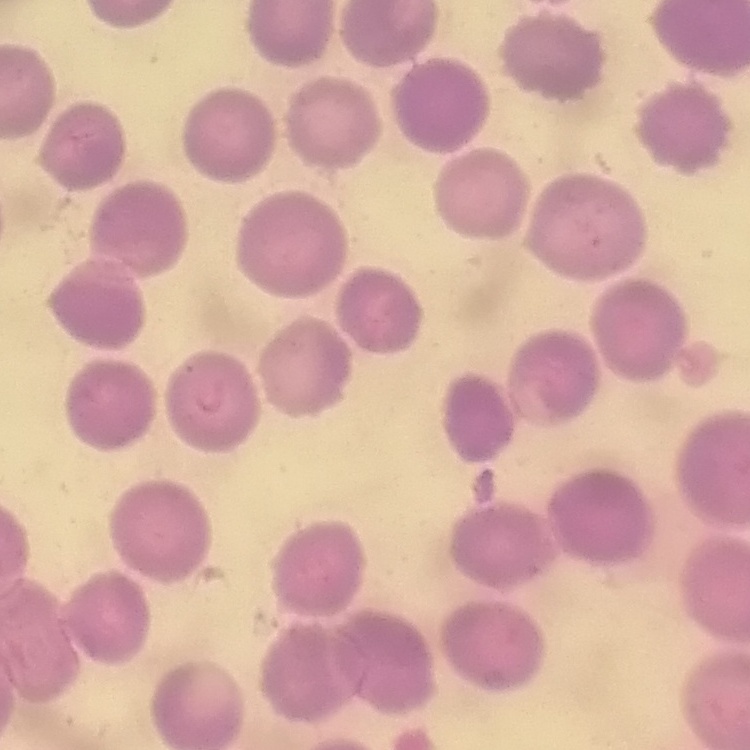 The erythrocytes show no rouleaux formation. One tile cut from a larger photomicrograph. Thin blood smear. Field's or Giemsa stain.